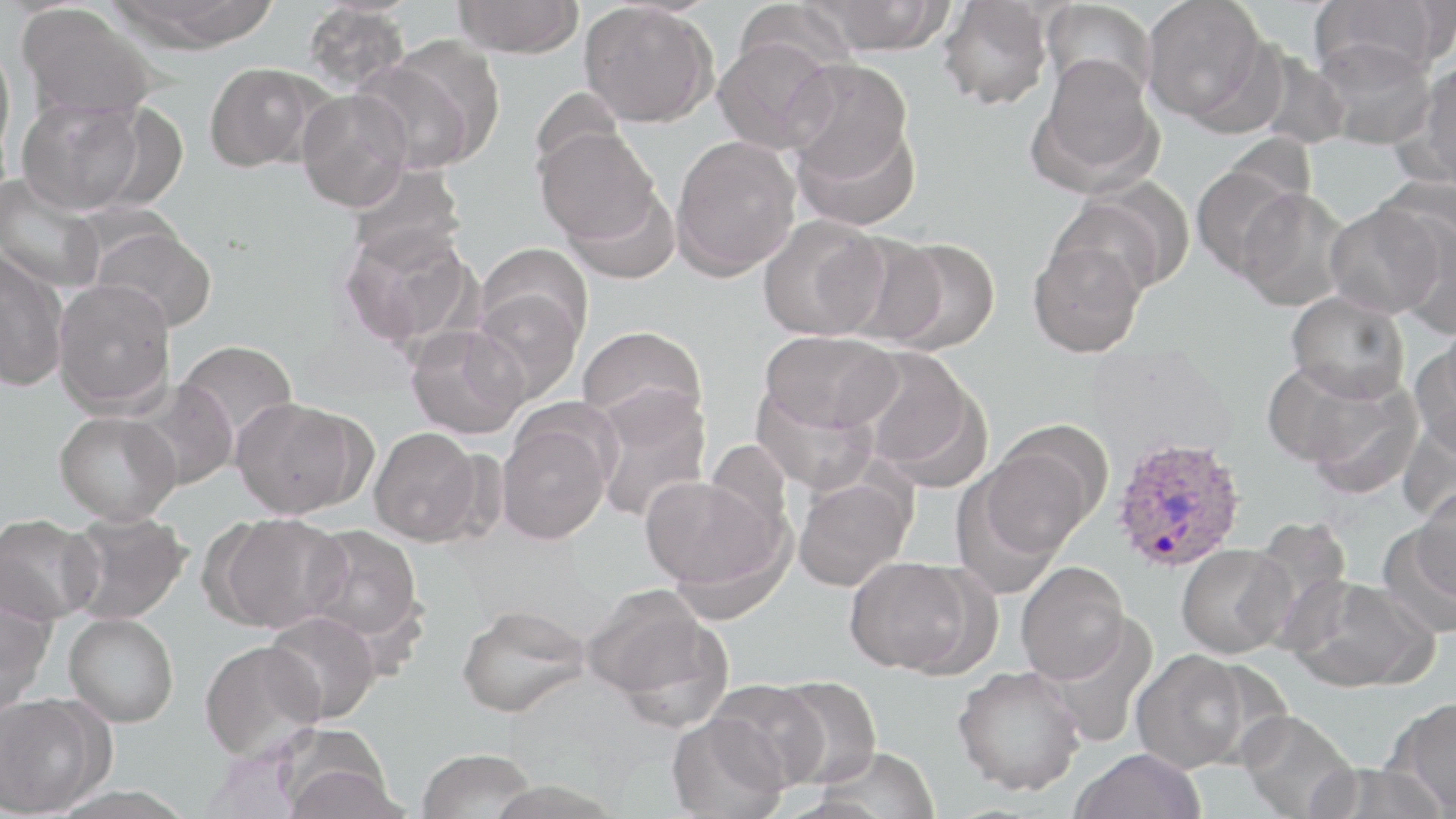
Summary:
  - Coordinate format: approximate bounding boxes as named x1/y1/x2/y2 corners in pixels
  - Uninfected red blood cell locations: (x1=109, y1=0, x2=280, y2=50), (x1=452, y1=0, x2=584, y2=58), (x1=733, y1=0, x2=857, y2=83), (x1=802, y1=0, x2=953, y2=55), (x1=1141, y1=0, x2=1269, y2=126), (x1=1308, y1=0, x2=1447, y2=84), (x1=937, y1=1, x2=1053, y2=111), (x1=1040, y1=1, x2=1158, y2=104), (x1=302, y1=2, x2=411, y2=95), (x1=579, y1=2, x2=717, y2=128), (x1=16, y1=4, x2=160, y2=122), (x1=713, y1=36, x2=837, y2=154), (x1=0, y1=37, x2=16, y2=171), (x1=1313, y1=41, x2=1437, y2=150), (x1=355, y1=44, x2=499, y2=172), (x1=1251, y1=49, x2=1351, y2=150), (x1=1030, y1=54, x2=1162, y2=194), (x1=784, y1=57, x2=915, y2=190), (x1=1412, y1=60, x2=1456, y2=186), (x1=204, y1=63, x2=321, y2=172), (x1=296, y1=90, x2=413, y2=212), (x1=17, y1=96, x2=148, y2=215), (x1=793, y1=116, x2=921, y2=231), (x1=534, y1=126, x2=659, y2=244), (x1=670, y1=135, x2=800, y2=278), (x1=345, y1=161, x2=467, y2=270), (x1=1190, y1=161, x2=1305, y2=281), (x1=0, y1=171, x2=106, y2=296), (x1=1053, y1=185, x2=1189, y2=298), (x1=564, y1=186, x2=681, y2=284), (x1=1235, y1=187, x2=1352, y2=311), (x1=1325, y1=201, x2=1444, y2=321), (x1=757, y1=215, x2=888, y2=342), (x1=1387, y1=215, x2=1456, y2=335), (x1=90, y1=223, x2=217, y2=333), (x1=339, y1=223, x2=477, y2=350), (x1=836, y1=232, x2=949, y2=348), (x1=877, y1=237, x2=1001, y2=353), (x1=1028, y1=237, x2=1146, y2=358), (x1=477, y1=243, x2=593, y2=351), (x1=0, y1=251, x2=69, y2=392), (x1=52, y1=279, x2=176, y2=415), (x1=471, y1=288, x2=584, y2=404), (x1=1286, y1=291, x2=1411, y2=402), (x1=405, y1=324, x2=529, y2=440), (x1=578, y1=326, x2=707, y2=431), (x1=760, y1=330, x2=900, y2=434), (x1=1415, y1=334, x2=1456, y2=458), (x1=175, y1=340, x2=298, y2=447), (x1=857, y1=348, x2=988, y2=486), (x1=1263, y1=360, x2=1416, y2=486), (x1=127, y1=380, x2=238, y2=491), (x1=751, y1=384, x2=879, y2=495), (x1=591, y1=389, x2=712, y2=522), (x1=231, y1=397, x2=369, y2=519), (x1=54, y1=410, x2=180, y2=525), (x1=496, y1=415, x2=613, y2=544), (x1=368, y1=426, x2=483, y2=545), (x1=979, y1=428, x2=1105, y2=558), (x1=952, y1=463, x2=1074, y2=598), (x1=640, y1=474, x2=786, y2=597), (x1=793, y1=475, x2=913, y2=591), (x1=1412, y1=482, x2=1456, y2=606), (x1=62, y1=511, x2=192, y2=624), (x1=212, y1=512, x2=348, y2=632), (x1=0, y1=514, x2=103, y2=625), (x1=1247, y1=515, x2=1352, y2=643), (x1=1377, y1=522, x2=1456, y2=640), (x1=301, y1=524, x2=423, y2=643), (x1=1176, y1=543, x2=1294, y2=659), (x1=845, y1=557, x2=978, y2=676), (x1=1016, y1=562, x2=1130, y2=683), (x1=1285, y1=576, x2=1435, y2=693), (x1=584, y1=585, x2=729, y2=721), (x1=0, y1=594, x2=54, y2=714), (x1=456, y1=604, x2=590, y2=718), (x1=263, y1=610, x2=381, y2=724), (x1=64, y1=613, x2=179, y2=727), (x1=1043, y1=617, x2=1159, y2=748), (x1=200, y1=639, x2=325, y2=761), (x1=1130, y1=649, x2=1253, y2=773), (x1=953, y1=664, x2=1085, y2=796), (x1=768, y1=676, x2=882, y2=788), (x1=707, y1=681, x2=829, y2=790), (x1=0, y1=694, x2=105, y2=817), (x1=1391, y1=697, x2=1456, y2=815), (x1=1235, y1=709, x2=1359, y2=819), (x1=666, y1=713, x2=789, y2=819), (x1=278, y1=740, x2=401, y2=819), (x1=811, y1=747, x2=939, y2=819), (x1=417, y1=748, x2=537, y2=819), (x1=1070, y1=748, x2=1206, y2=819), (x1=1308, y1=761, x2=1449, y2=819), (x1=480, y1=779, x2=626, y2=818)
  - Plasmodium ovale-infected red blood cell locations: (x1=1112, y1=436, x2=1246, y2=573)
  - Slide-level diagnosis: Plasmodium ovale
  - Magnification: 1000x
  - Field of view: one of a larger specimen
  - Preparation: thin blood film
  - Image size: 1456×819 pixels
  - Stain: May-Grünwald-Giemsa
  - Modality: optical microscopy